Identify the parasite.
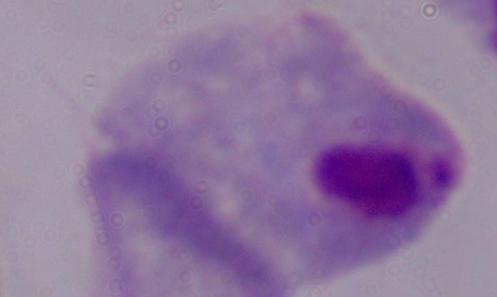

This is a trichomonad.

Summary:
  - Magnification: 1000x
  - Modality: micrograph